Comment on the morphology of the erythrocytes.
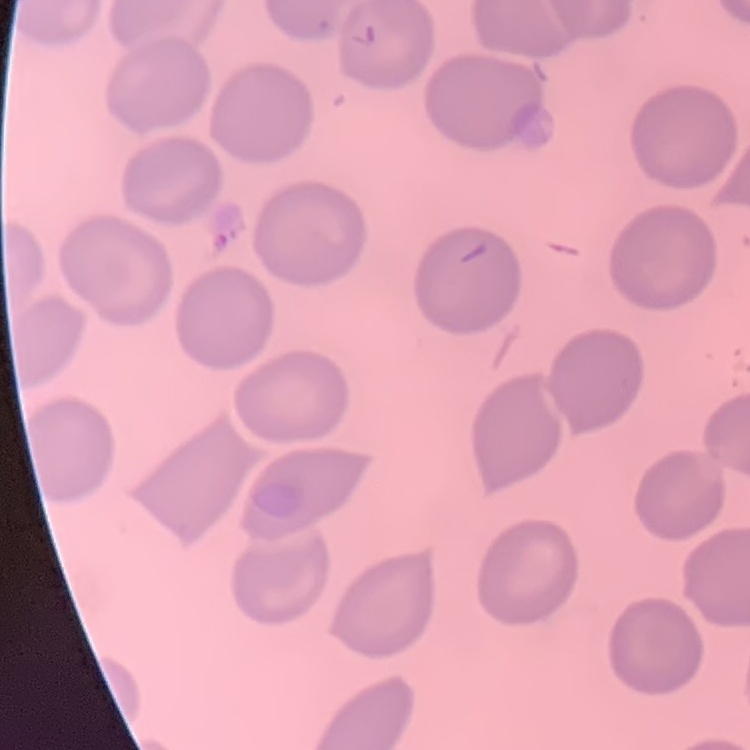

They show no rouleaux formation.

Square crop of a larger photomicrograph. Thin blood smear. Stained with either Field's or Giemsa.